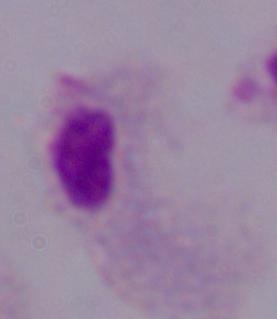

modality = micrograph
identification = trichomonad
magnification = 1000x